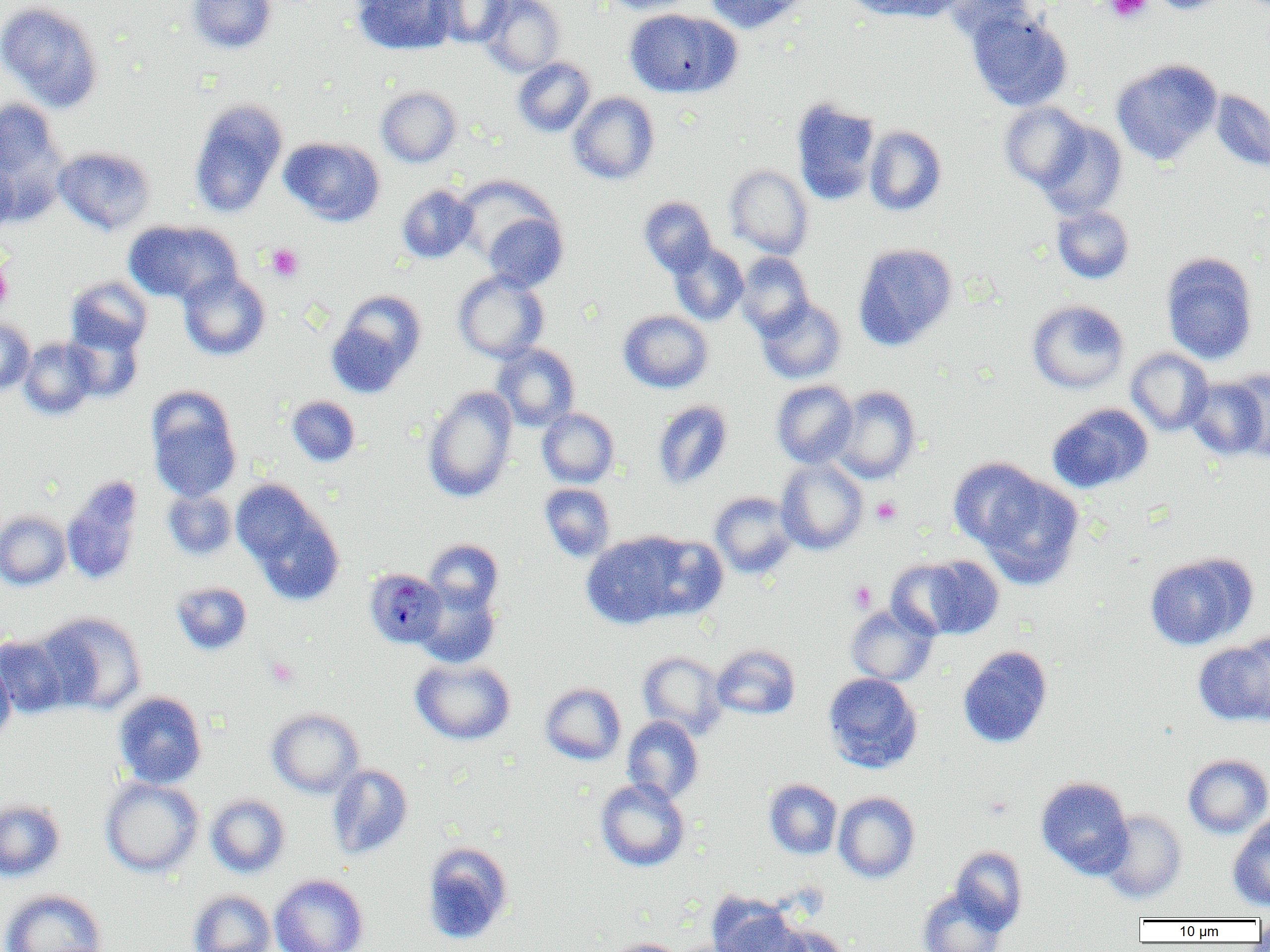
Summary:
  - Coordinate format: approximate bounding boxes as (x1,y1)-(x2,y2) corner pairs in pixels
  - Uninfected red blood cell locations: (186,0)-(277,54), (352,0)-(458,54), (434,0)-(513,47), (480,0)-(566,77), (600,0)-(699,14), (703,0)-(810,34), (845,0)-(950,21), (941,0)-(1038,43), (1148,0)-(1235,14), (0,1)-(104,112), (624,8)-(740,98), (966,8)-(1073,111), (512,57)-(595,137), (1111,58)-(1222,165), (376,86)-(462,167), (1209,89)-(1270,173), (568,92)-(660,184), (791,98)-(881,205), (0,99)-(67,215), (189,99)-(287,218), (999,102)-(1091,190), (1036,120)-(1127,219), (864,126)-(947,216), (280,136)-(385,226), (54,146)-(156,235), (0,158)-(18,234), (725,164)-(814,258), (454,175)-(558,269), (397,184)-(477,263), (639,196)-(717,277), (1051,205)-(1134,283), (480,209)-(569,291), (124,220)-(241,304), (669,243)-(748,325), (852,243)-(958,351), (736,252)-(814,338), (1160,252)-(1259,365), (179,270)-(271,360), (453,271)-(549,363), (65,276)-(152,355), (326,289)-(427,397), (755,298)-(846,384), (1027,299)-(1129,393), (618,310)-(713,393), (0,319)-(35,396), (64,324)-(144,402), (19,338)-(99,419), (492,343)-(580,431), (1126,348)-(1214,436), (1186,376)-(1268,461), (771,380)-(858,468), (832,385)-(921,484), (422,386)-(518,502), (146,389)-(242,503), (286,396)-(360,466), (652,400)-(733,489), (1047,403)-(1153,493), (537,408)-(619,487), (947,457)-(1047,550), (776,458)-(868,555), (978,475)-(1085,589), (62,477)-(143,585), (233,481)-(344,604), (539,483)-(615,561), (162,489)-(237,560), (710,491)-(798,579), (0,510)-(71,590), (581,533)-(687,629), (636,534)-(728,621), (425,539)-(504,614), (1145,553)-(1255,650), (902,555)-(1005,640), (171,582)-(252,656), (414,584)-(501,669), (845,604)-(939,686), (39,611)-(147,716), (1234,632)-(1270,722), (0,634)-(70,718), (1193,637)-(1270,726), (711,644)-(800,720), (957,645)-(1053,748), (637,651)-(727,739), (0,657)-(16,743), (410,658)-(515,745), (822,673)-(923,773), (540,682)-(626,765), (113,691)-(207,789), (266,707)-(365,798), (622,716)-(704,804), (1183,754)-(1270,838), (326,764)-(413,860), (1036,776)-(1133,879), (100,777)-(204,878), (595,778)-(691,872), (764,779)-(842,859), (833,791)-(920,883), (205,793)-(290,878), (0,798)-(66,881), (1099,810)-(1188,901), (1228,814)-(1270,911), (421,841)-(514,944), (950,845)-(1028,933), (269,874)-(369,952), (917,887)-(1008,952), (0,889)-(108,952), (187,889)-(276,952), (707,891)-(805,952), (1253,915)-(1270,944), (765,924)-(851,952), (601,937)-(686,952), (669,939)-(756,952)
  - Plasmodium malariae-infected red blood cell locations: (365,571)-(443,646)
  - Platelet locations: (1104,0)-(1152,23), (265,243)-(305,282), (0,256)-(12,314), (871,497)-(901,525), (849,581)-(877,612), (265,656)-(299,688)
  - Slide-level diagnosis: Plasmodium malariae
  - Preparation: thin blood smear
  - Magnification: 1000x
  - Image size: 1270×952 pixels
  - Field of view: one of a larger specimen
  - Modality: light microscopy